Name the parasite shown.
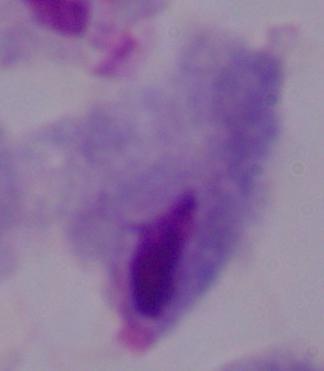

This is a trichomonad.

Summary:
  - Magnification: 1000x
  - Modality: micrograph